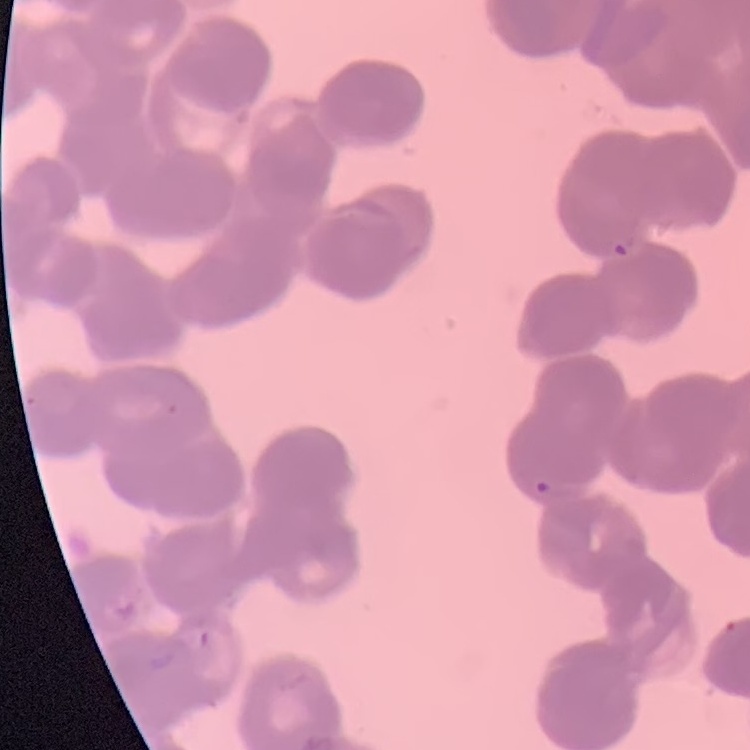
erythrocyte morphology = rouleaux formation
image type = one tile cut from a larger photomicrograph
preparation = thin blood smear
stain = Field's or Giemsa